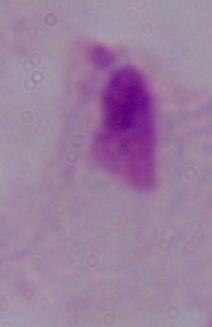
1000x magnification. Micrograph. A trichomonad is seen.